Comment on the morphology of the erythrocytes.
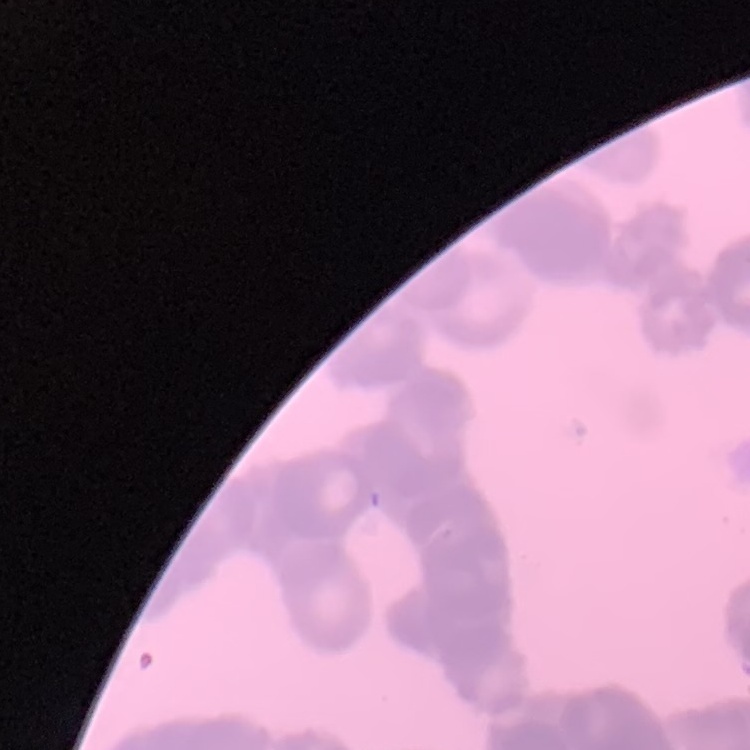
Rouleaux formation.

image type = square crop of a larger photomicrograph
stain = Field's or Giemsa
preparation = thin peripheral smear